State the blood parasite species.
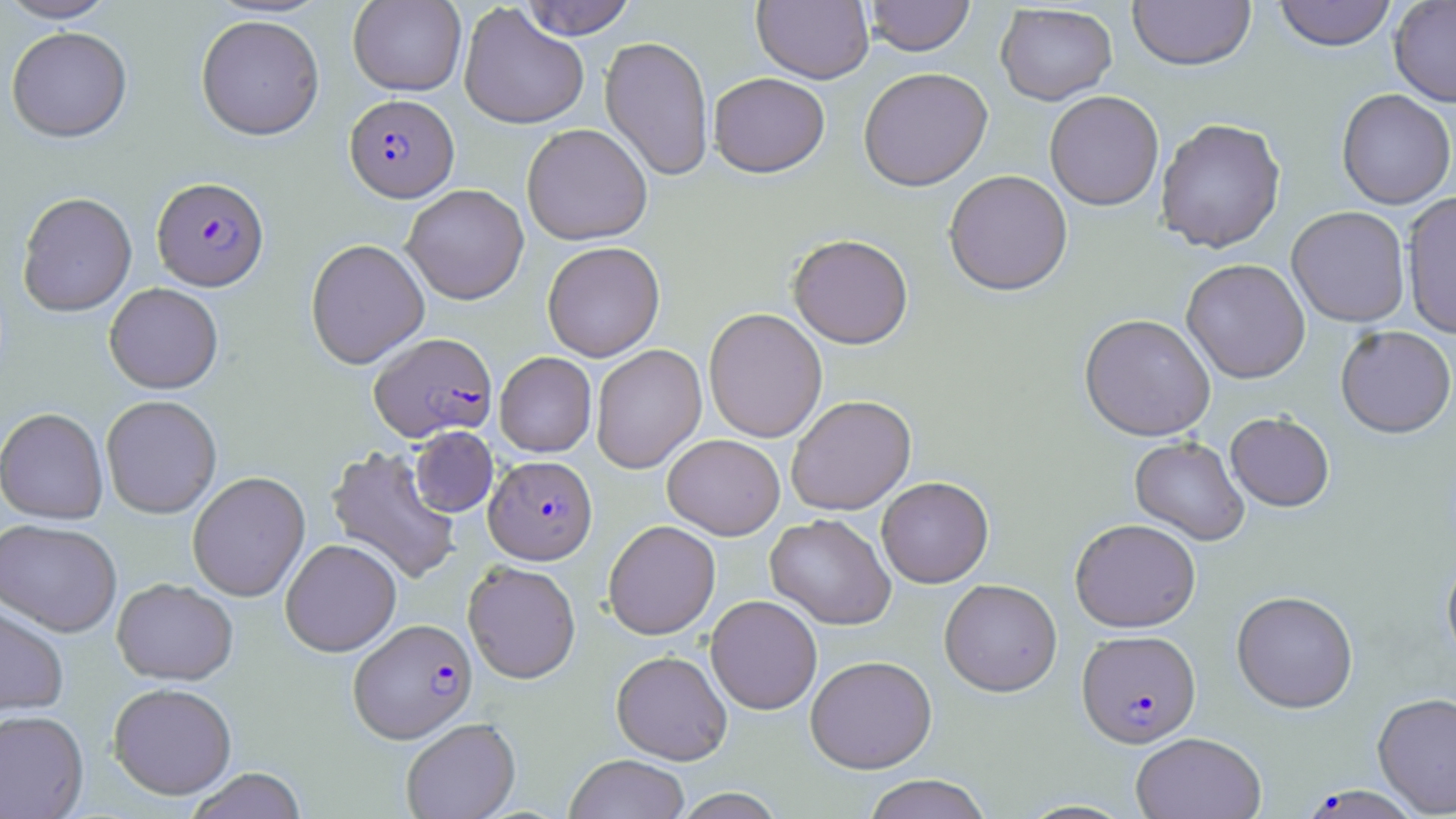
Plasmodium falciparum.

Approximate bounding boxes as (x1,y1)-(x2,y2) corner pairs in pixels. Uninfected red blood cell locations: (0,0)-(118,23), (348,0)-(466,96), (519,0)-(637,39), (753,0)-(873,84), (864,0)-(975,56), (1128,0)-(1255,71), (1272,0)-(1398,51), (1389,0)-(1456,107), (459,3)-(590,129), (995,3)-(1117,105), (195,14)-(325,141), (5,26)-(132,143), (600,35)-(714,182), (858,66)-(993,191), (708,72)-(830,177), (1336,88)-(1455,209), (1045,91)-(1164,210), (1155,117)-(1286,253), (522,123)-(652,245), (943,169)-(1073,296), (402,184)-(529,304), (1402,191)-(1456,340), (17,192)-(137,317), (1286,206)-(1410,327), (788,233)-(913,349), (305,238)-(430,369), (542,241)-(665,362), (1181,258)-(1310,383), (104,283)-(223,394), (704,308)-(828,443), (1079,313)-(1215,441), (1335,325)-(1455,438), (591,344)-(707,474), (495,351)-(597,457), (786,394)-(916,515), (101,395)-(222,518), (0,408)-(109,524), (1225,412)-(1335,511), (409,427)-(498,517), (662,434)-(785,540), (1129,436)-(1249,545), (325,444)-(461,585), (187,471)-(310,601), (877,476)-(993,587), (765,513)-(896,630), (1069,518)-(1201,632), (0,519)-(122,637), (603,520)-(721,640), (281,538)-(401,657), (1441,555)-(1456,669), (462,561)-(581,684), (112,578)-(238,686), (939,578)-(1062,696), (1231,590)-(1358,713), (705,595)-(822,714), (0,601)-(69,717), (611,650)-(732,765), (805,655)-(937,773), (108,682)-(237,801), (1372,691)-(1456,816), (0,709)-(89,818), (401,718)-(520,819), (1131,732)-(1267,819), (565,753)-(690,819), (184,768)-(307,819), (861,774)-(993,819), (671,788)-(787,819). Plasmodium falciparum-infected red blood cell locations: (344,94)-(459,202), (152,176)-(269,291), (369,332)-(497,442), (484,455)-(597,564), (349,618)-(477,743), (1077,629)-(1201,747), (1303,784)-(1421,819). Thin blood film. Captured at 1000x magnification. Image is 1456×819 pixels. May-Grünwald-Giemsa stain. Optical microscopy. One field of a larger specimen.